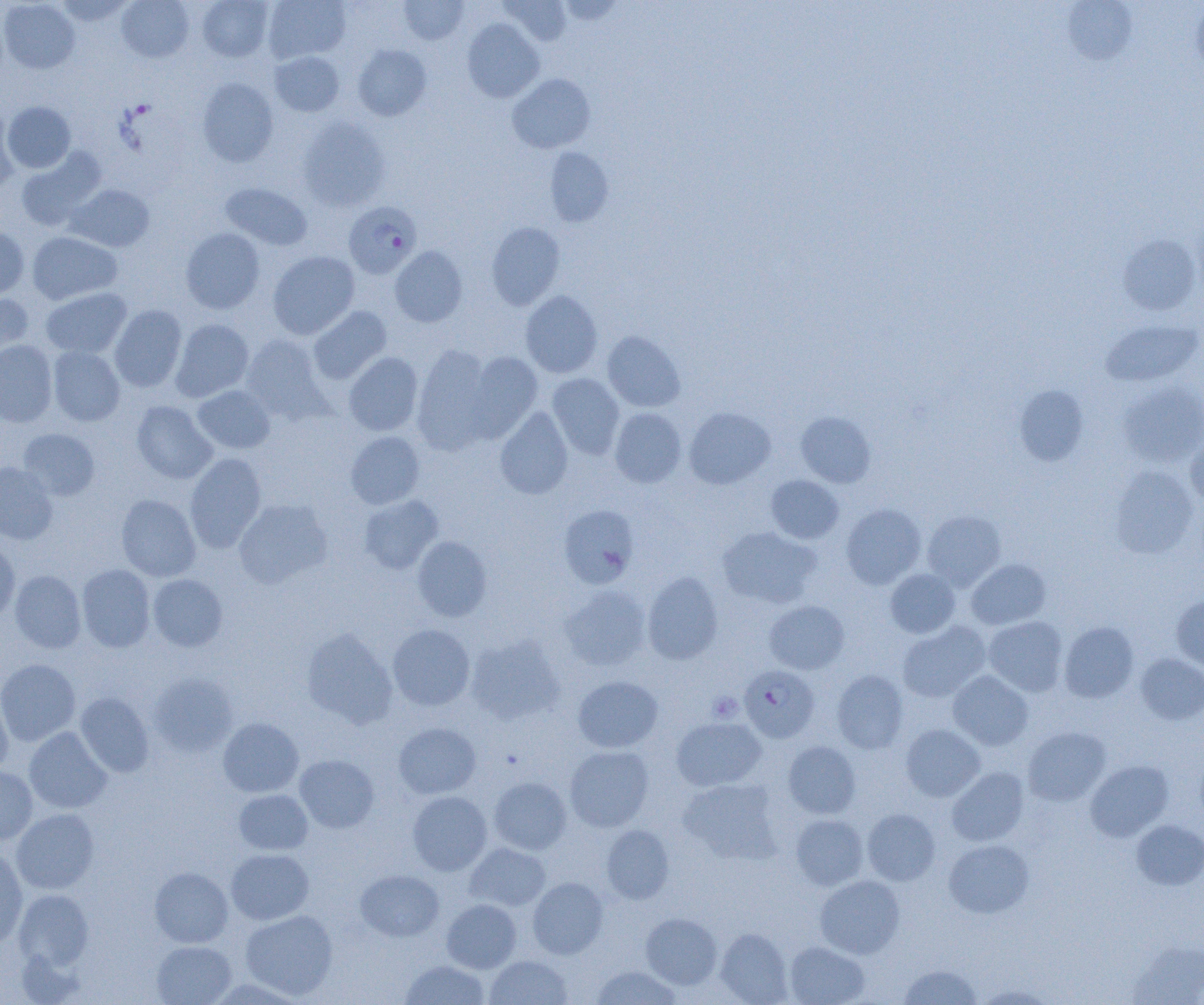

Summary:
  - Coordinate format: approximate bounding boxes as (x1, y1, x2, y2) in pixels
  - Platelet locations: (707, 692, 743, 722)
  - Plasmodium falciparum-infected red blood cell locations: (344, 201, 422, 279), (739, 665, 820, 742)
  - Uninfected red blood cell locations: (0, 0, 80, 74), (54, 0, 135, 26), (116, 0, 194, 63), (197, 0, 274, 62), (262, 0, 350, 63), (398, 0, 469, 45), (501, 0, 572, 46), (1060, 1, 1138, 64), (1191, 2, 1204, 79), (462, 18, 544, 102), (353, 45, 432, 121), (269, 51, 344, 117), (507, 73, 596, 153), (197, 77, 279, 167), (3, 101, 76, 173), (0, 105, 19, 190), (298, 117, 391, 211), (545, 148, 613, 226), (16, 149, 105, 231), (219, 182, 312, 250), (66, 184, 155, 252), (486, 222, 565, 310), (0, 225, 29, 297), (181, 227, 265, 314), (27, 232, 122, 305), (1117, 233, 1202, 316), (390, 246, 467, 327), (267, 251, 360, 339), (40, 287, 132, 358), (520, 290, 603, 378), (0, 294, 34, 365), (109, 305, 187, 392), (308, 306, 391, 384), (171, 318, 254, 401), (1100, 319, 1203, 387), (602, 331, 685, 412), (240, 335, 330, 423), (0, 340, 57, 427), (412, 344, 498, 452), (48, 346, 125, 426), (464, 351, 543, 440), (343, 352, 423, 436), (546, 373, 624, 460), (1117, 381, 1204, 467), (192, 385, 275, 454), (1014, 385, 1089, 466), (131, 401, 217, 484), (495, 406, 573, 499), (610, 407, 687, 488), (684, 407, 776, 490), (795, 411, 876, 488), (18, 428, 100, 500), (346, 431, 425, 509), (1185, 434, 1204, 509), (184, 452, 267, 552), (0, 461, 59, 544), (1109, 465, 1198, 559), (766, 475, 844, 544), (116, 494, 201, 581), (358, 494, 443, 574), (233, 498, 333, 588), (558, 503, 640, 589), (841, 504, 926, 589), (922, 510, 1006, 591), (717, 527, 820, 609), (412, 536, 492, 621), (0, 537, 20, 623), (966, 558, 1052, 630), (77, 564, 155, 652), (885, 568, 961, 638), (10, 570, 86, 653), (642, 572, 723, 664), (148, 574, 227, 651), (559, 585, 652, 671), (1171, 595, 1204, 673), (764, 600, 849, 674), (983, 616, 1068, 696), (897, 621, 990, 702), (1058, 621, 1139, 703), (387, 624, 476, 711), (301, 627, 397, 728), (465, 634, 566, 725), (1135, 653, 1204, 725), (0, 659, 80, 746), (831, 670, 908, 754), (948, 670, 1034, 750), (148, 672, 237, 757), (572, 675, 663, 753), (0, 690, 13, 776), (75, 693, 154, 777), (218, 717, 303, 797), (671, 718, 766, 791), (393, 722, 481, 799), (900, 724, 985, 802), (1022, 726, 1111, 806), (24, 727, 112, 814), (783, 740, 861, 818), (564, 745, 653, 832), (294, 754, 379, 834), (1085, 760, 1173, 842), (0, 766, 38, 845), (947, 768, 1028, 846), (488, 776, 572, 854), (678, 778, 783, 864), (234, 789, 313, 855), (407, 791, 492, 875), (11, 808, 99, 894), (862, 808, 940, 885), (791, 814, 868, 890), (1131, 819, 1204, 890), (601, 825, 674, 904), (943, 839, 1034, 918), (465, 842, 551, 912), (0, 845, 28, 947), (226, 848, 314, 924), (150, 867, 233, 947), (355, 869, 444, 941), (815, 875, 905, 959), (528, 877, 608, 959), (13, 889, 94, 970), (442, 899, 521, 972), (240, 909, 337, 999), (641, 913, 722, 989), (714, 928, 793, 1004), (1127, 939, 1204, 1005), (151, 941, 236, 1004), (784, 941, 869, 1005), (485, 955, 572, 1005), (401, 959, 487, 1005), (898, 964, 982, 1004), (591, 965, 682, 1004), (208, 977, 308, 1005), (975, 984, 1056, 1004)
  - Slide-level diagnosis: Plasmodium falciparum
  - Magnification: 1000x
  - Image size: 1204×1005 pixels
  - Modality: light microscopy
  - Field of view: one of a larger specimen
  - Preparation: thin blood smear